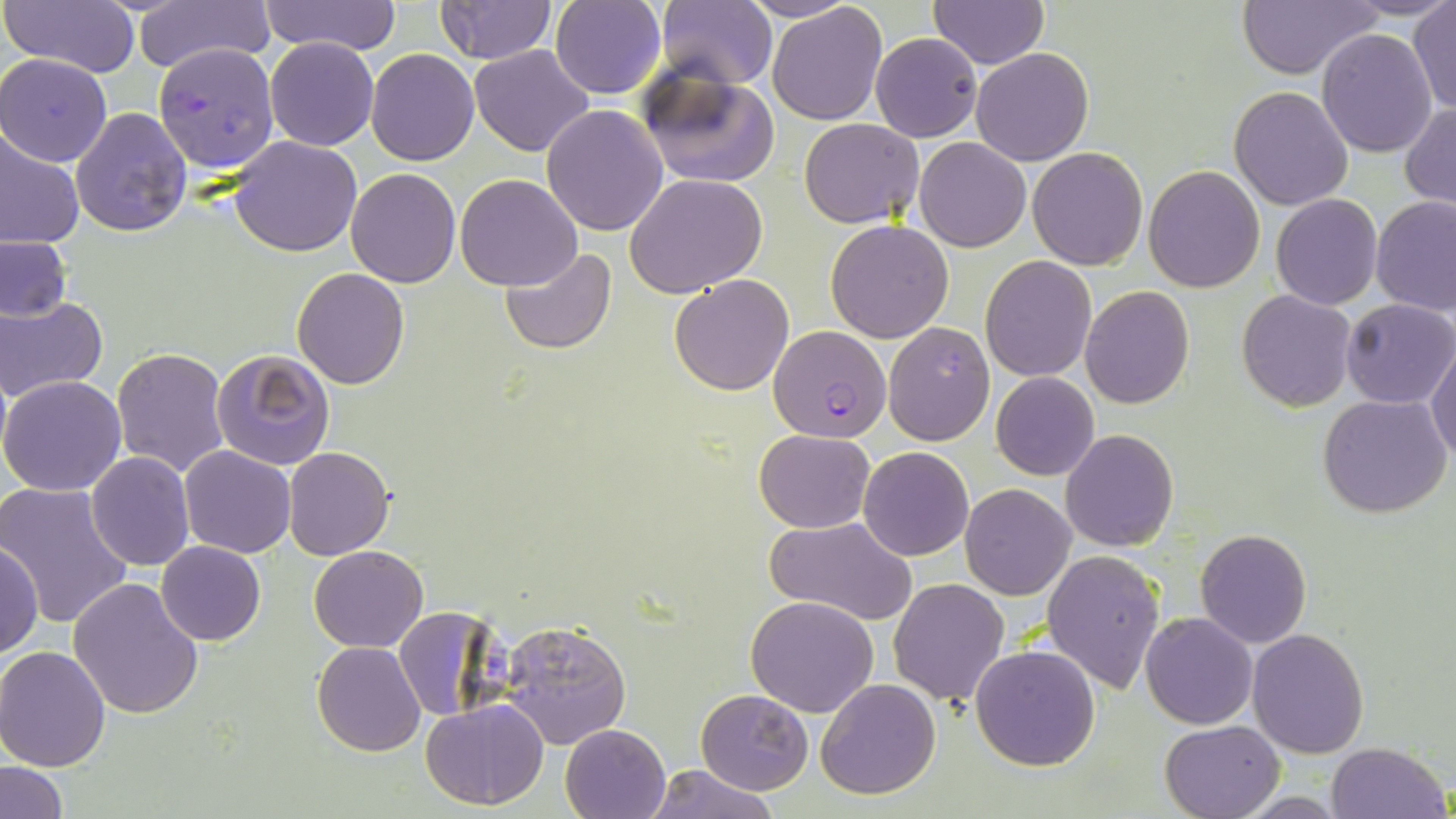 Approximate bounding boxes as (x1, y1, x2, y2) in pixels. Plasmodium falciparum-infected red blood cell locations: (152, 41, 278, 174), (768, 326, 893, 444). Uninfected red blood cell locations: (2, 0, 142, 78), (259, 0, 402, 55), (433, 0, 557, 64), (657, 0, 778, 91), (733, 0, 863, 23), (927, 0, 1050, 70), (1233, 0, 1384, 79), (135, 1, 272, 74), (549, 1, 666, 99), (768, 2, 888, 123), (1408, 4, 1455, 114), (1317, 28, 1437, 157), (869, 32, 982, 141), (264, 37, 380, 151), (468, 44, 595, 158), (971, 47, 1093, 166), (367, 48, 479, 165), (0, 53, 114, 167), (638, 68, 781, 188), (1228, 86, 1355, 211), (1402, 103, 1456, 214), (540, 104, 668, 236), (70, 107, 193, 237), (799, 118, 925, 228), (0, 128, 82, 251), (228, 135, 363, 257), (915, 138, 1032, 253), (1027, 146, 1148, 269), (1143, 165, 1265, 293), (346, 168, 461, 287), (455, 174, 583, 292), (626, 174, 769, 296), (1271, 194, 1382, 309), (1371, 195, 1456, 315), (825, 219, 954, 343), (0, 235, 72, 323), (500, 248, 617, 354), (979, 256, 1097, 383), (292, 266, 410, 388), (669, 274, 795, 396), (1079, 286, 1194, 409), (1236, 291, 1358, 411), (1, 295, 108, 402), (1340, 299, 1455, 408), (883, 321, 997, 447), (1429, 340, 1456, 463), (112, 347, 231, 479), (211, 349, 335, 470), (990, 371, 1099, 481), (0, 374, 127, 496), (1319, 393, 1453, 517), (753, 428, 875, 531), (1060, 429, 1179, 551), (179, 445, 296, 559), (283, 446, 395, 560), (858, 446, 974, 561), (85, 451, 195, 570), (960, 483, 1076, 599), (0, 484, 134, 632), (764, 516, 918, 625), (1194, 530, 1311, 648), (1, 541, 44, 659), (157, 541, 266, 646), (309, 545, 428, 652), (1041, 549, 1165, 694), (66, 577, 206, 719), (887, 578, 1010, 707), (745, 596, 878, 718), (393, 606, 497, 724), (1140, 612, 1258, 730), (500, 619, 631, 748), (1246, 628, 1369, 758), (312, 640, 425, 756), (970, 643, 1101, 771), (1, 645, 113, 770), (815, 679, 941, 801), (697, 690, 814, 794), (421, 700, 549, 809), (1158, 719, 1284, 819), (560, 722, 672, 819), (1326, 741, 1450, 819), (3, 760, 67, 818), (644, 764, 779, 819). Slide-level diagnosis: Plasmodium falciparum. Image is 1456×819 pixels. One field of a larger specimen. Captured at 1000x magnification. Thin blood smear. Optical microscopy. May-Grünwald-Giemsa stain.